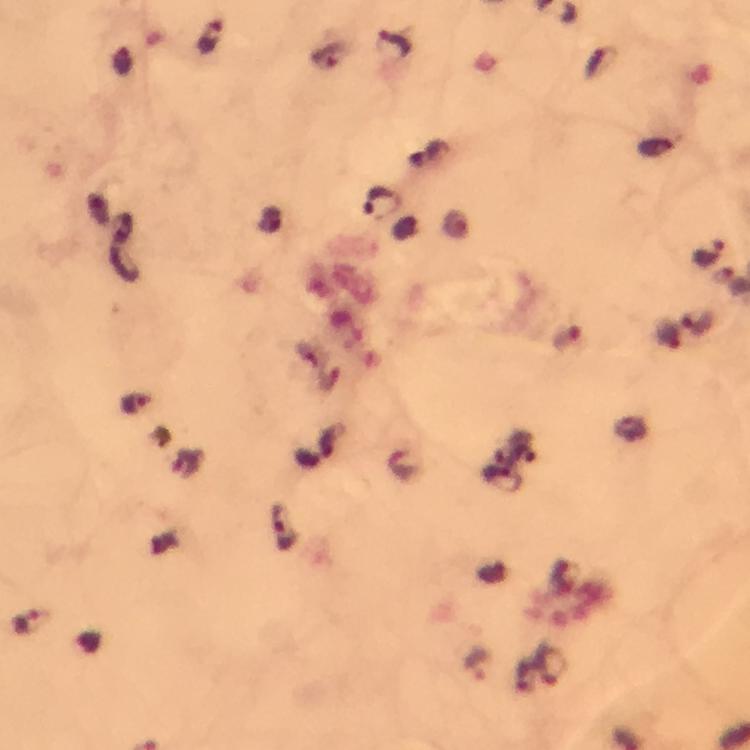
Approximate centers as (x, y) in pixels. Plasmodium parasite locations: (212, 38), (328, 57), (380, 200), (708, 254), (698, 325), (570, 339), (136, 404), (503, 480), (285, 527), (28, 624), (479, 664), (552, 664). 100x magnification. A crop from one field of view. Thick blood smear. Photographed with a smartphone mounted on the microscope. Image is 750×750 pixels. Immersion oil applied. From a malaria diagnostic workup. Giemsa stain.